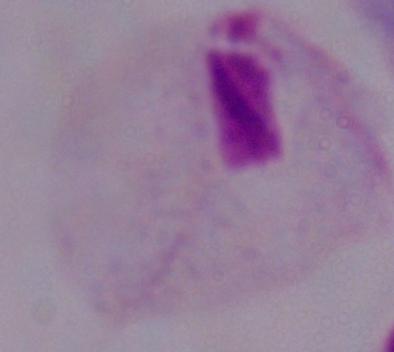

A trichomonad is seen. Captured at 1000x magnification. Photomicrograph.